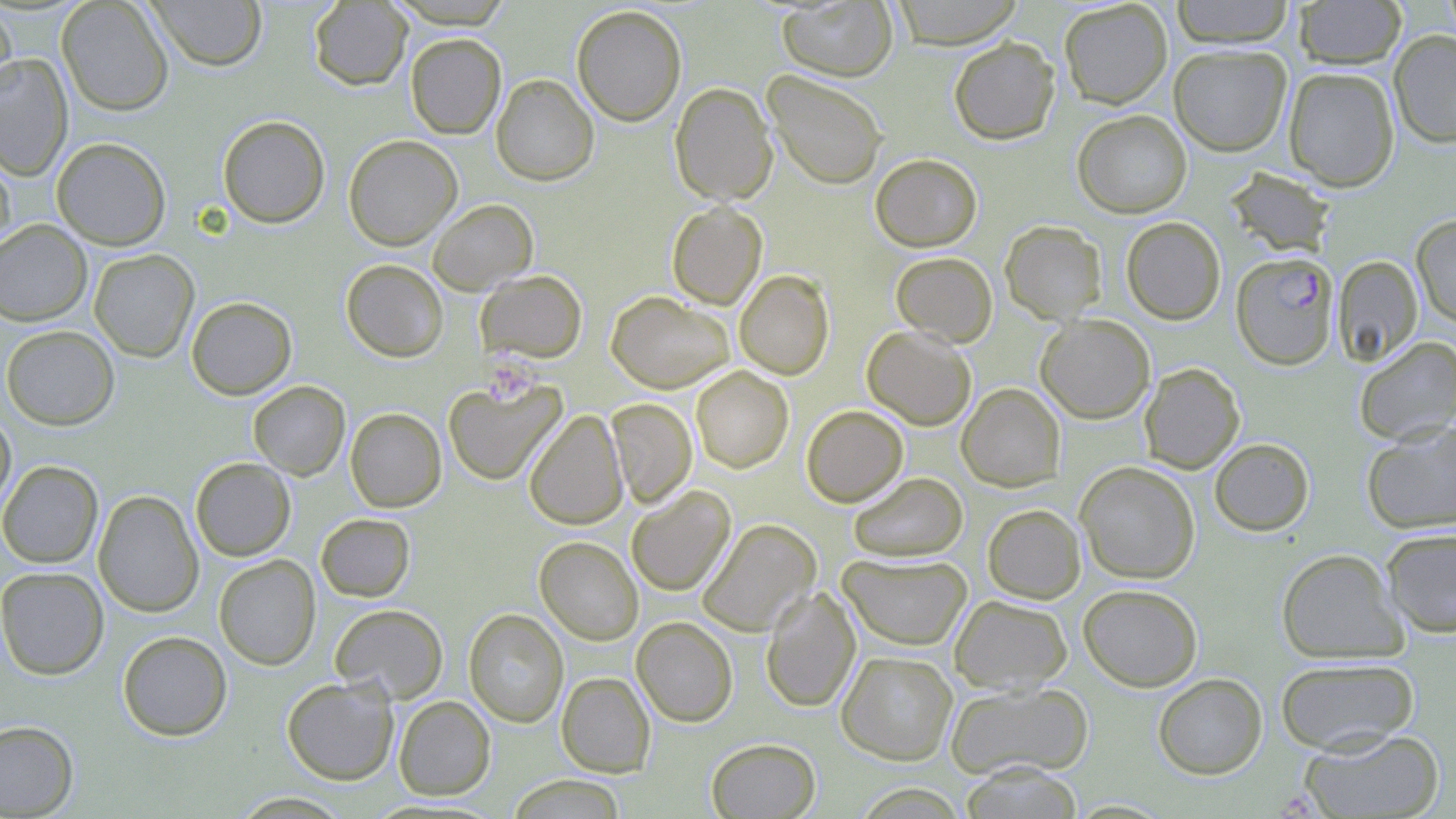
slide-level diagnosis = Plasmodium falciparum
magnification = 1000x
modality = optical microscopy
platelet locations = approximate bounding boxes as (x1, y1, x2, y2) in pixels: (482, 356, 539, 403)
image size = 1456×819 pixels
preparation = thin blood smear
field of view = single
uninfected red blood cell locations = approximate bounding boxes as (x1, y1, x2, y2) in pixels: (57, 0, 174, 116), (147, 0, 267, 71), (386, 0, 515, 28), (776, 0, 898, 82), (890, 0, 1025, 49), (1058, 0, 1172, 109), (1170, 0, 1295, 48), (1293, 0, 1407, 69), (308, 1, 412, 90), (0, 2, 17, 106), (571, 5, 687, 126), (1389, 30, 1456, 148), (405, 33, 506, 139), (949, 36, 1060, 145), (1168, 44, 1292, 156), (0, 52, 73, 179), (1283, 67, 1400, 192), (764, 70, 888, 189), (491, 73, 599, 186), (670, 82, 777, 205), (1072, 110, 1192, 218), (217, 115, 330, 228), (343, 134, 462, 251), (52, 137, 171, 250), (0, 148, 16, 255), (870, 153, 982, 252), (1224, 167, 1337, 259), (427, 199, 538, 295), (666, 202, 767, 309), (1411, 215, 1456, 327), (1121, 216, 1225, 325), (0, 220, 92, 326), (1000, 220, 1106, 324), (89, 249, 200, 362), (890, 252, 998, 347), (1333, 255, 1423, 366), (340, 259, 449, 362), (734, 269, 834, 379), (476, 270, 587, 362), (605, 290, 734, 393), (186, 296, 297, 399), (1035, 314, 1155, 423), (1, 325, 120, 430), (862, 325, 976, 430), (1354, 337, 1456, 445), (1139, 362, 1245, 473), (691, 366, 794, 473), (443, 378, 566, 486), (248, 381, 350, 480), (957, 383, 1065, 491), (606, 398, 697, 507), (801, 405, 908, 506), (345, 407, 446, 512), (0, 408, 16, 519), (524, 410, 628, 530), (1361, 420, 1456, 534), (1209, 438, 1314, 536), (190, 457, 295, 561), (0, 460, 103, 568), (1075, 461, 1200, 583), (847, 471, 968, 562), (626, 486, 735, 596), (93, 489, 204, 617), (982, 504, 1086, 603), (316, 513, 415, 602), (697, 519, 821, 636), (1380, 528, 1456, 637), (535, 536, 643, 645), (1276, 548, 1406, 664), (837, 552, 973, 650), (214, 554, 321, 670), (0, 567, 109, 680), (1078, 583, 1202, 691), (760, 586, 860, 713), (949, 595, 1072, 693), (329, 603, 448, 703), (463, 608, 568, 727), (632, 616, 737, 727), (117, 630, 232, 741), (837, 651, 958, 765), (1274, 657, 1420, 755), (556, 672, 655, 777), (1153, 673, 1267, 779), (281, 677, 399, 785), (944, 681, 1094, 778), (393, 695, 495, 800), (0, 720, 78, 817), (1299, 727, 1446, 818), (706, 737, 821, 818), (958, 762, 1085, 819), (506, 775, 627, 818), (230, 791, 354, 818)
stain = May-Grünwald-Giemsa
Plasmodium falciparum-infected red blood cell locations = approximate bounding boxes as (x1, y1, x2, y2) in pixels: (1231, 252, 1338, 370)